Give the extent of all Plasmodium ovale-infected red blood cells.
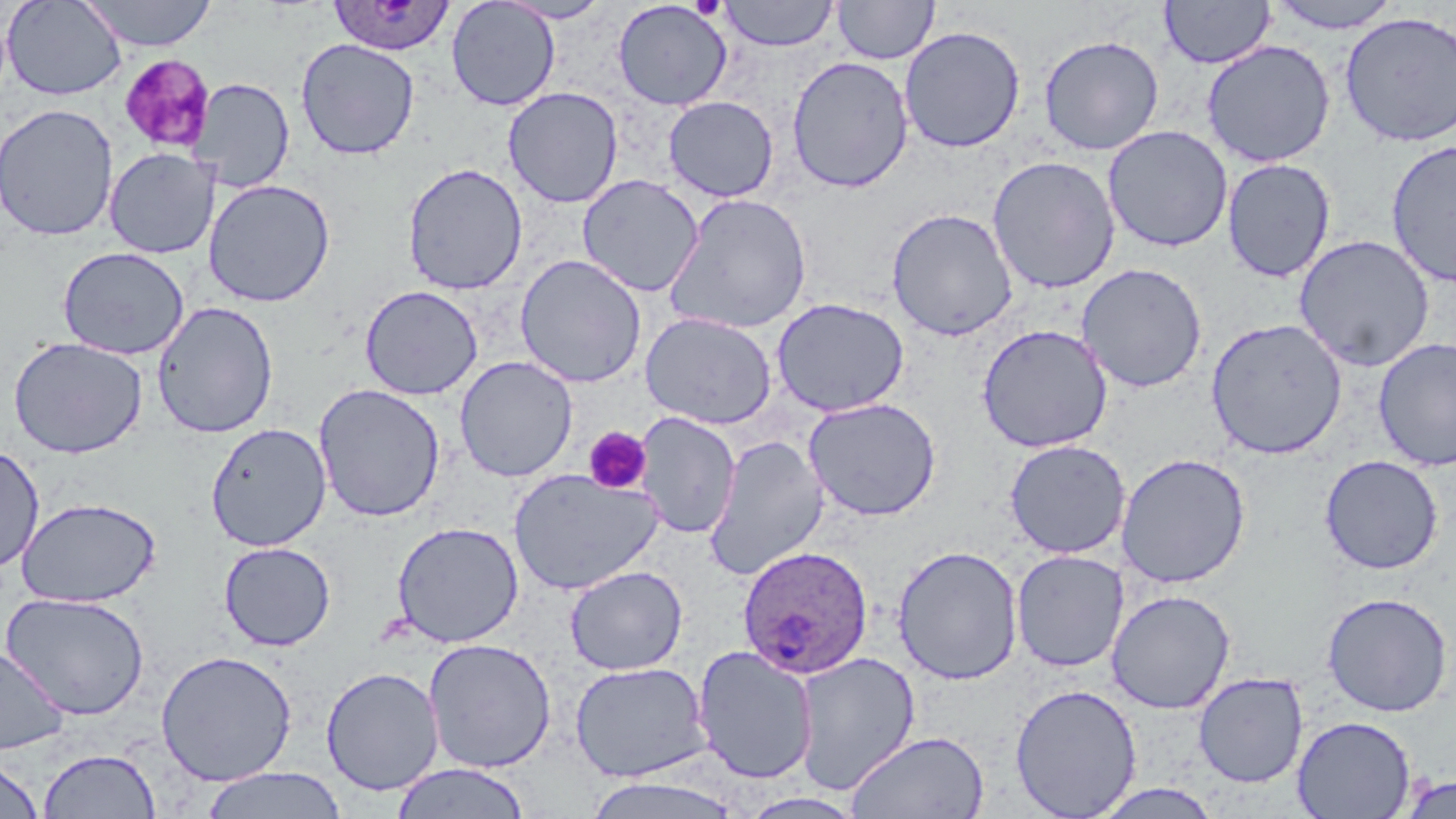
Approximate bounding boxes as (x1, y1, x2, y2) in pixels.
Plasmodium ovale-infected red blood cells: (326, 1, 457, 57), (736, 545, 874, 679).

slide-level diagnosis = Plasmodium ovale
field of view = one of a larger specimen
modality = optical microscopy
uninfected red blood cell locations = approximate bounding boxes as (x1, y1, x2, y2) in pixels: (2, 0, 128, 101), (78, 0, 218, 51), (446, 0, 561, 111), (496, 0, 614, 23), (833, 0, 939, 64), (1159, 0, 1275, 69), (1267, 0, 1406, 33), (612, 1, 733, 111), (718, 1, 839, 51), (1339, 12, 1456, 147), (899, 25, 1025, 153), (1038, 34, 1164, 155), (296, 38, 420, 160), (1201, 40, 1336, 167), (786, 55, 914, 193), (195, 78, 295, 192), (503, 87, 624, 208), (663, 96, 779, 201), (0, 103, 119, 241), (1102, 125, 1233, 252), (1385, 139, 1456, 287), (104, 147, 219, 259), (987, 155, 1121, 293), (1222, 158, 1336, 283), (402, 162, 528, 295), (577, 174, 705, 297), (203, 179, 336, 307), (663, 191, 813, 334), (886, 208, 1018, 342), (1295, 234, 1434, 372), (57, 247, 189, 360), (514, 254, 647, 388), (1076, 262, 1208, 394), (359, 285, 483, 400), (771, 297, 910, 416), (152, 301, 279, 438), (641, 312, 777, 429), (1206, 318, 1348, 459), (976, 323, 1113, 453), (8, 336, 148, 459), (1373, 337, 1456, 472), (455, 356, 578, 482), (313, 383, 446, 522), (803, 397, 942, 521), (633, 412, 740, 539), (205, 422, 332, 551), (704, 434, 829, 579), (1004, 439, 1131, 559), (0, 443, 45, 575), (1116, 452, 1251, 589), (1319, 454, 1444, 575), (507, 468, 664, 594), (15, 497, 162, 607), (391, 521, 524, 647), (218, 541, 336, 651), (892, 544, 1024, 685), (1011, 549, 1129, 672), (564, 565, 688, 675), (1105, 589, 1237, 713), (1321, 591, 1453, 717), (1, 592, 151, 721), (423, 638, 557, 773), (0, 645, 69, 755), (692, 645, 818, 784), (155, 649, 298, 786), (792, 652, 920, 794), (569, 661, 711, 783), (320, 666, 445, 796), (1193, 672, 1308, 788), (1009, 683, 1143, 818), (1292, 716, 1417, 818), (846, 730, 989, 818), (38, 748, 161, 818), (0, 755, 44, 818), (390, 763, 531, 819), (200, 767, 348, 819), (584, 773, 744, 818), (1398, 774, 1456, 818), (1088, 782, 1227, 818)
magnification = 1000x
stain = May-Grünwald-Giemsa
preparation = thin blood film
platelet locations = approximate bounding boxes as (x1, y1, x2, y2) in pixels: (118, 54, 216, 153), (583, 426, 652, 495)
image size = 1456×819 pixels